Locate platelets.
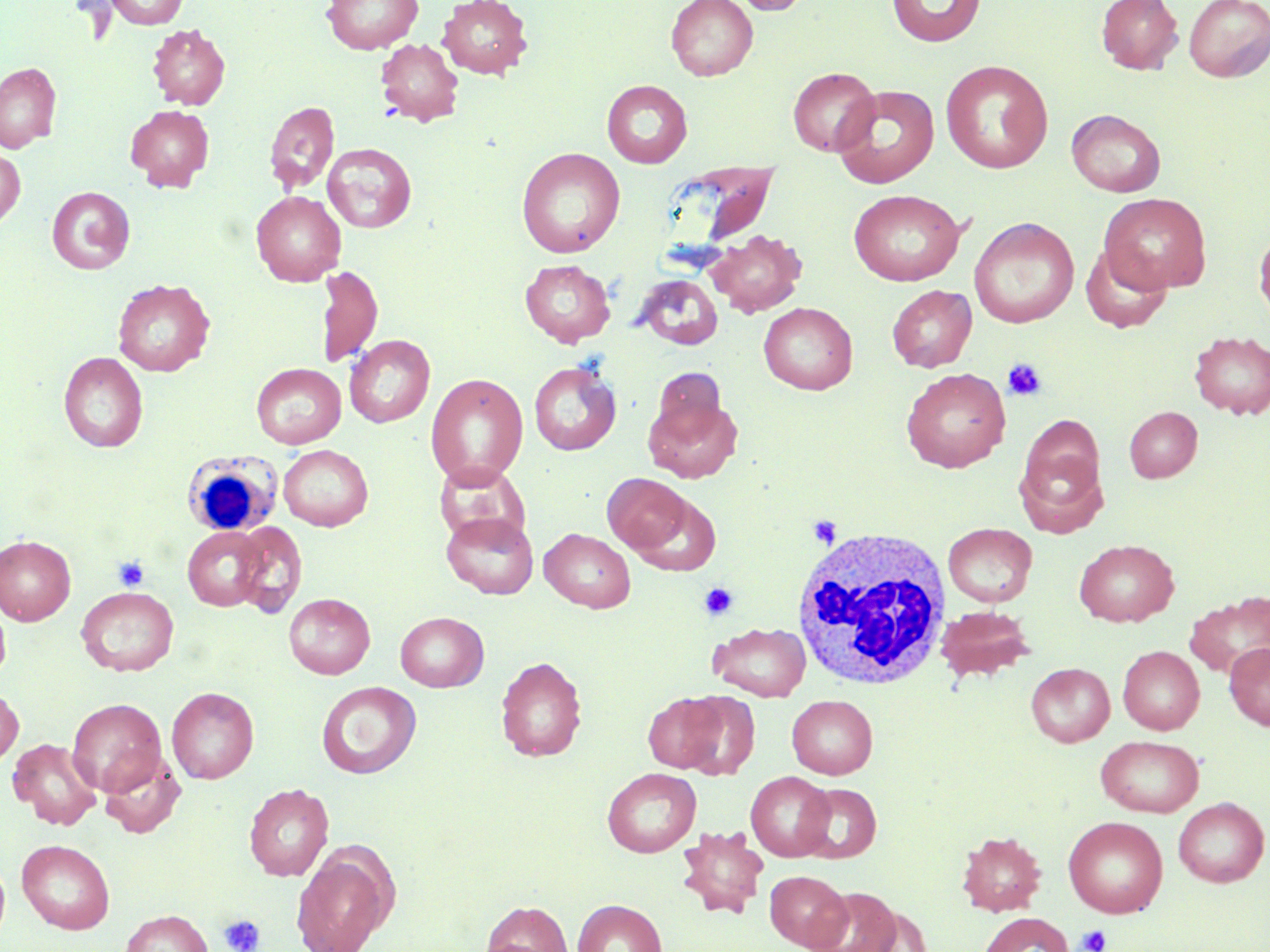
Approximate bounding boxes as [x1, y1, x2, y2] in pixels.
Platelets: [1002, 358, 1047, 401], [807, 516, 842, 547], [113, 555, 150, 592], [699, 582, 738, 620], [219, 914, 265, 952], [1077, 925, 1111, 952].

slide-level diagnosis = no evidence of blood parasites
white blood cell locations = approximate bounding boxes as [x1, y1, x2, y2] in pixels: [182, 450, 282, 537], [791, 526, 953, 691]
modality = optical microscopy
magnification = 1000x
image size = 1270×952 pixels
field of view = one of a larger specimen
stain = May-Grünwald-Giemsa
preparation = thin blood smear
uninfected red blood cell locations = approximate bounding boxes as [x1, y1, x2, y2] in pixels: [104, 0, 189, 29], [322, 0, 423, 54], [438, 0, 533, 79], [665, 0, 758, 81], [728, 0, 812, 15], [886, 0, 986, 48], [1096, 0, 1183, 74], [1184, 0, 1270, 82], [148, 24, 230, 109], [376, 38, 463, 126], [940, 60, 1053, 174], [0, 62, 61, 152], [787, 67, 880, 156], [602, 80, 693, 168], [832, 84, 940, 189], [264, 100, 340, 193], [125, 105, 215, 191], [1067, 109, 1165, 197], [322, 142, 417, 232], [0, 146, 25, 229], [516, 147, 626, 258], [666, 165, 780, 249], [47, 186, 135, 274], [848, 189, 964, 286], [251, 191, 346, 286], [1099, 193, 1211, 294], [970, 217, 1079, 328], [1254, 227, 1270, 325], [707, 229, 807, 317], [1082, 244, 1172, 333], [519, 259, 616, 346], [316, 264, 383, 368], [635, 274, 723, 350], [113, 279, 214, 376], [887, 284, 976, 372], [758, 301, 858, 394], [1189, 331, 1270, 419], [344, 334, 435, 428], [59, 351, 148, 452], [529, 361, 621, 456], [252, 363, 346, 449], [901, 367, 1010, 472], [651, 368, 728, 443], [425, 372, 528, 487], [643, 394, 742, 483], [1124, 406, 1202, 482], [1015, 428, 1109, 535], [278, 444, 373, 531], [433, 460, 529, 545], [602, 473, 691, 553], [632, 494, 723, 576], [441, 511, 539, 599], [231, 522, 307, 617], [943, 522, 1037, 607], [183, 526, 267, 611], [539, 528, 635, 613], [0, 535, 75, 625], [1074, 539, 1179, 627], [76, 586, 179, 676], [1185, 590, 1270, 678], [284, 593, 375, 679], [0, 597, 11, 685], [935, 605, 1035, 682], [395, 611, 489, 691], [709, 622, 811, 700], [1224, 642, 1270, 731], [1118, 645, 1204, 734], [495, 656, 587, 762], [1026, 663, 1115, 747], [316, 681, 421, 779], [0, 686, 23, 770], [167, 686, 258, 783], [677, 691, 760, 779], [643, 692, 727, 772], [787, 695, 877, 779], [67, 697, 167, 797], [1095, 735, 1204, 817], [7, 738, 101, 829], [99, 752, 185, 838], [602, 767, 701, 857], [746, 771, 834, 861], [244, 783, 334, 881], [798, 783, 882, 863], [1172, 797, 1269, 887], [1063, 816, 1168, 918], [677, 826, 768, 918], [957, 831, 1047, 916], [17, 839, 115, 934], [291, 848, 394, 952], [0, 857, 10, 944], [765, 870, 851, 950], [810, 886, 902, 952], [573, 898, 666, 952], [481, 900, 573, 952], [121, 909, 212, 952], [979, 912, 1074, 952]